Point out malaria parasites and leukocytes.
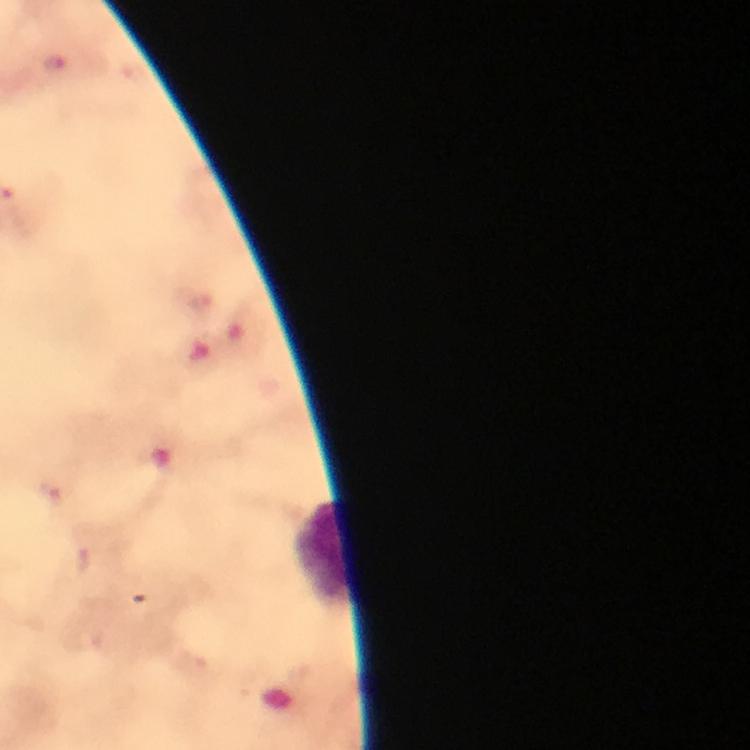

Approximate centers as [x, y] in pixels.
Malaria parasites: [200, 303], [51, 493], [81, 557].
Leukocytes: [325, 553].

immersion oil = used
image size = 750×750 pixels
cropped from = one field of view
context = from a malaria diagnostic workup
magnification = 100x
preparation = thick blood film
capture = smartphone camera through the microscope
stain = Giemsa